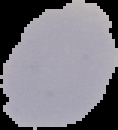
Image is 118×130 pixels. Cell region segmented out of the field of view; the surrounding area is masked to black. From a thin blood film. Result: negative for Plasmodium parasites.